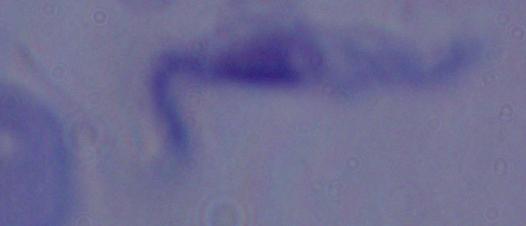
modality: micrograph
magnification: 1000x
identification: trypanosome